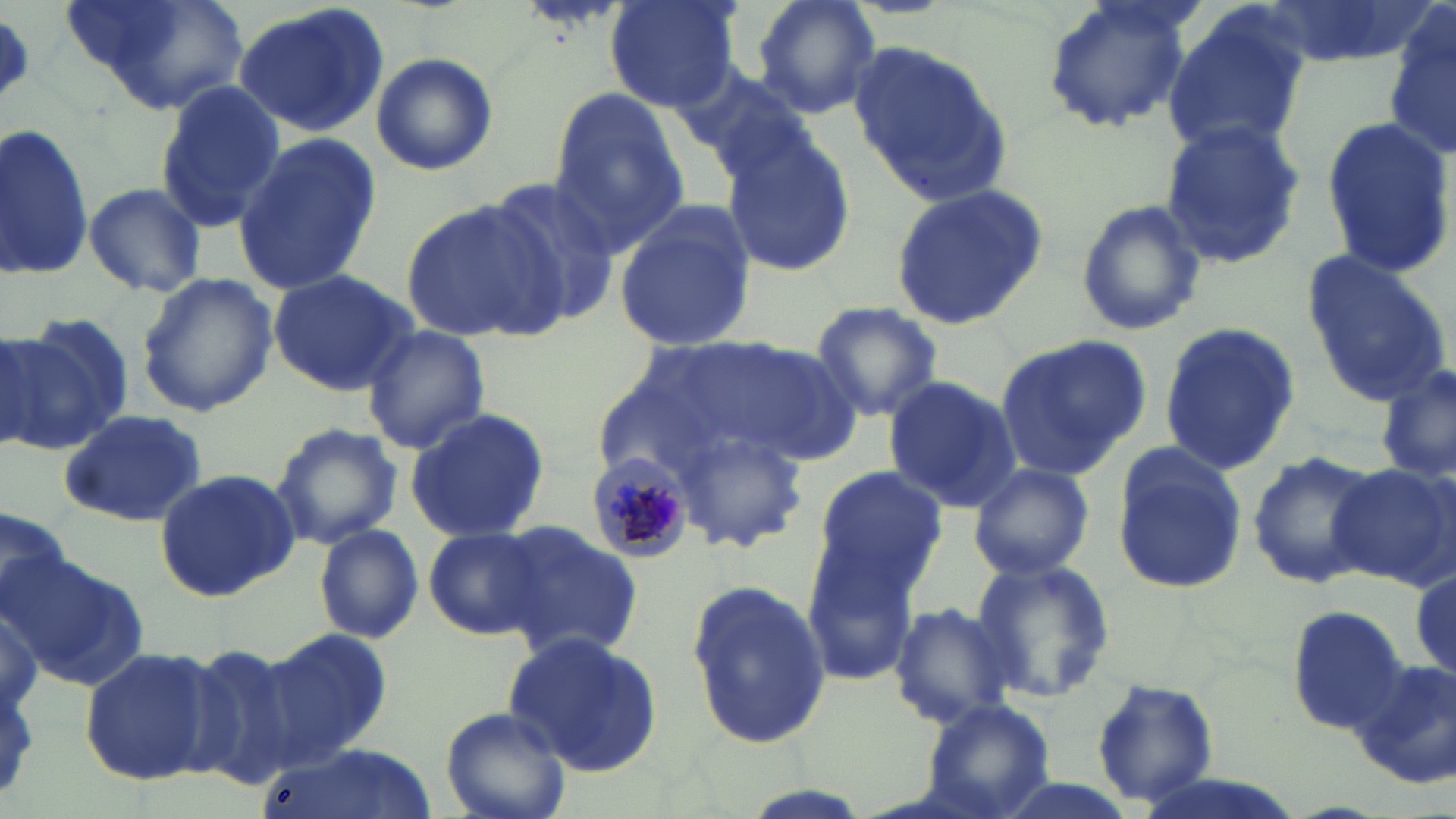

{
  "slide_level_diagnosis": "Plasmodium malariae",
  "magnification": "1000x",
  "plasmodium_malariae_infected_red_blood_cell_locations": "approximate bounding boxes as (x1, y1, x2, y2) in pixels: (588, 451, 696, 562)",
  "field_of_view": "single",
  "modality": "light microscopy",
  "stain": "May-Grünwald-Giemsa",
  "uninfected_red_blood_cell_locations": "approximate bounding boxes as (x1, y1, x2, y2) in pixels: (65, 0, 251, 115), (605, 0, 741, 112), (751, 0, 883, 119), (1040, 0, 1197, 133), (1259, 1, 1421, 69), (232, 3, 389, 139), (1161, 3, 1313, 159), (1384, 9, 1456, 160), (0, 12, 33, 108), (852, 43, 1011, 205), (369, 52, 499, 177), (676, 63, 812, 179), (154, 81, 286, 231), (546, 92, 692, 254), (1318, 116, 1454, 279), (1, 120, 95, 283), (1158, 120, 1304, 270), (721, 133, 856, 281), (232, 135, 378, 299), (486, 176, 626, 329), (82, 181, 207, 298), (888, 185, 1052, 328), (400, 196, 567, 344), (1073, 199, 1207, 338), (614, 203, 757, 353), (1299, 250, 1453, 405), (268, 268, 419, 396), (136, 273, 279, 418), (808, 301, 945, 422), (7, 315, 134, 449), (1158, 323, 1302, 476), (361, 325, 490, 454), (688, 334, 865, 466), (994, 335, 1150, 472), (2, 336, 57, 451), (1377, 361, 1453, 488), (882, 376, 1023, 510), (403, 409, 551, 542), (59, 411, 213, 529), (671, 421, 809, 555), (269, 422, 403, 550), (1110, 443, 1246, 596), (1244, 450, 1378, 587), (1329, 460, 1455, 590), (968, 461, 1095, 578), (807, 466, 947, 602), (155, 468, 299, 602), (0, 508, 71, 618), (499, 521, 641, 659), (313, 524, 425, 645), (424, 525, 550, 641), (800, 537, 924, 686), (5, 552, 151, 691), (971, 554, 1115, 704), (1410, 558, 1455, 682), (682, 576, 835, 751), (1284, 602, 1408, 730), (889, 603, 1016, 729), (255, 625, 394, 772), (502, 630, 666, 777), (179, 641, 300, 792), (79, 645, 222, 787), (1349, 659, 1456, 789), (1092, 679, 1221, 805), (918, 700, 1056, 819), (440, 706, 570, 819), (262, 743, 435, 819)",
  "image_size": "1456×819 pixels",
  "preparation": "thin blood smear"
}